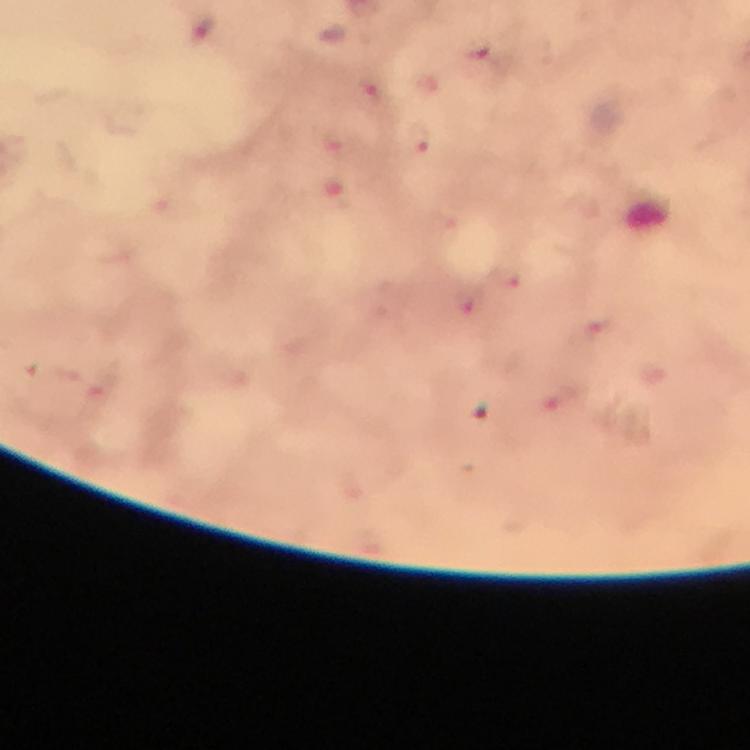
Approximate centers as (x, y) in pixels.
Summary:
  - Plasmodium parasite locations: (203, 33), (486, 66), (374, 92), (420, 138), (508, 282), (468, 300), (595, 330), (565, 399)
  - Magnification: 100x
  - Cropped from: a single field of view
  - Image size: 750×750 pixels
  - Preparation: thick blood smear
  - Capture: smartphone camera through the microscope
  - Immersion oil: applied
  - Context: from a diagnostic examination for malaria
  - Stain: Giemsa